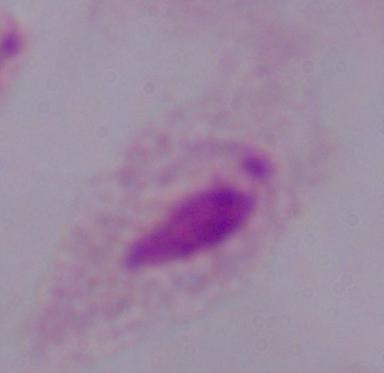
identification = trichomonad
magnification = 1000x
modality = photomicrograph